Classify this cell by malaria status.
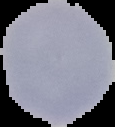

Uninfected.

Cell region segmented out of the field of view; the surrounding area is masked to black. Image is 115×127 pixels. From a thin blood smear.